Identify the cell.
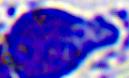

This is a leukocyte.

Micrograph. Captured at 400x magnification.